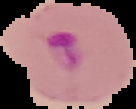

Segmented cell region on a black background. From a thin blood film. Image is 136×109 pixels. Malaria status: parasitized.